Outline each uninfected red blood cell.
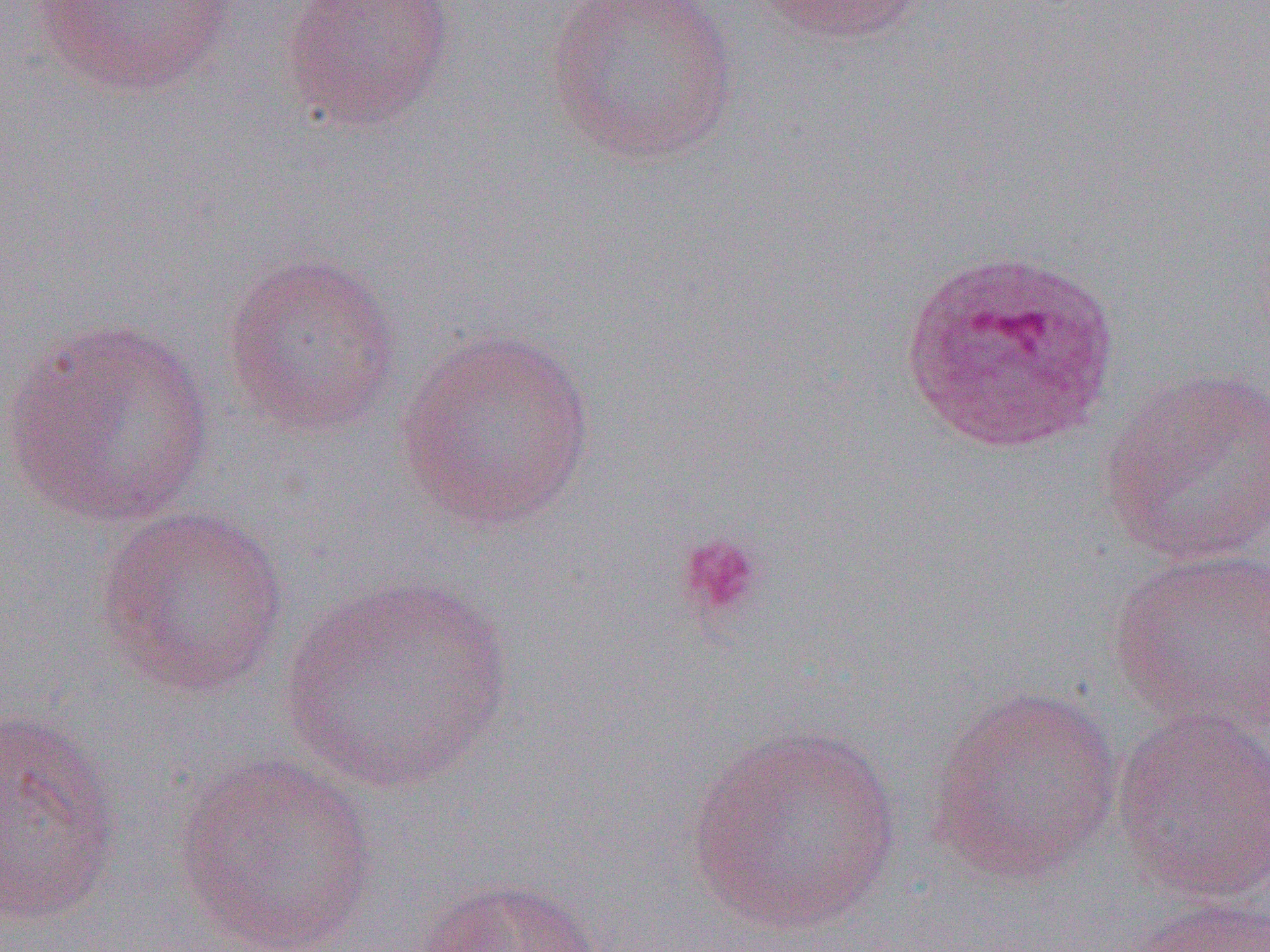
Approximate bounding boxes as named x1/y1/x2/y2 corners in pixels.
Uninfected red blood cells: (x1=29, y1=0, x2=243, y2=100), (x1=281, y1=0, x2=457, y2=133), (x1=545, y1=0, x2=741, y2=167), (x1=746, y1=0, x2=933, y2=45), (x1=221, y1=250, x2=402, y2=436), (x1=2, y1=316, x2=215, y2=528), (x1=397, y1=325, x2=596, y2=531), (x1=1099, y1=365, x2=1270, y2=567), (x1=95, y1=504, x2=289, y2=698), (x1=1106, y1=545, x2=1270, y2=733), (x1=279, y1=573, x2=512, y2=794), (x1=927, y1=687, x2=1123, y2=886), (x1=0, y1=705, x2=123, y2=926), (x1=1109, y1=707, x2=1270, y2=903), (x1=688, y1=722, x2=902, y2=934), (x1=173, y1=753, x2=381, y2=952), (x1=412, y1=876, x2=605, y2=952), (x1=1127, y1=894, x2=1270, y2=952).

Summary:
  - Plasmodium ovale-infected red blood cell locations: (x1=899, y1=247, x2=1123, y2=457)
  - Platelet locations: (x1=675, y1=530, x2=767, y2=623)
  - Slide-level diagnosis: Plasmodium ovale
  - Field of view: single
  - Modality: light microscopy
  - Preparation: thin blood smear
  - Magnification: 1000x
  - Image size: 1270×952 pixels